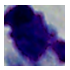 1000x magnification. A white blood cell is seen. Micrograph.